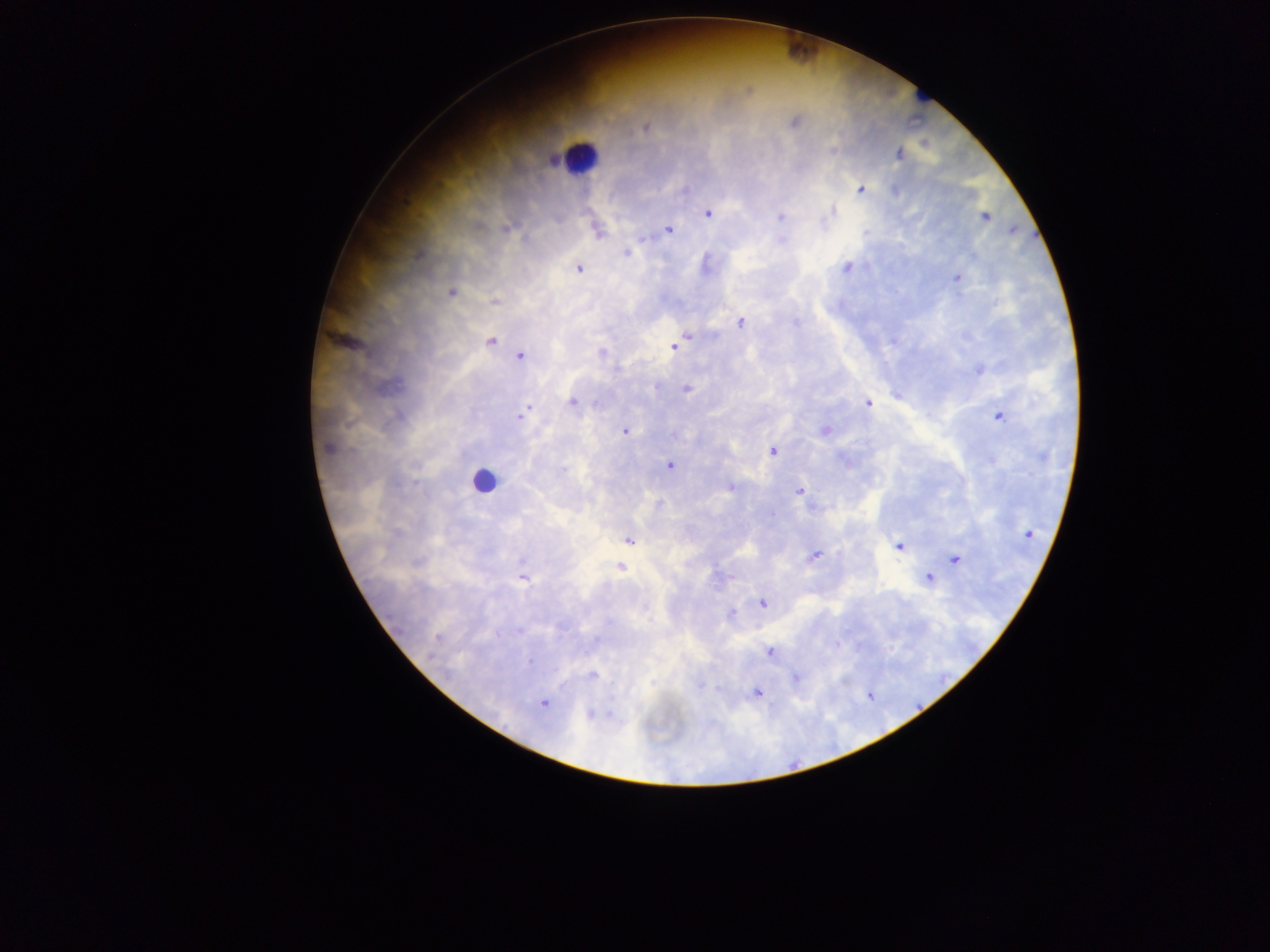
Approximate centers as x y in pixels.
Summary:
  - Leukocyte locations: 580 157; 483 481
  - Malaria parasite locations: 794 122; 646 128; 832 150; 899 154; 685 189; 862 190; 832 212; 708 213; 781 217; 985 217; 506 229; 1012 229; 668 230; 598 231; 625 253; 846 268; 578 269; 957 279; 451 293; 495 302; 741 322; 796 323; 687 336; 490 341; 674 346; 601 352; 520 356; 979 371; 686 389; 572 402; 868 403; 526 409; 521 415; 998 417; 624 431; 825 431; 673 435; 328 448; 773 451; 669 466; 563 470; 730 487; 799 491; 660 504; 771 514; 1027 535; 629 541; 899 546; 814 556; 956 560; 620 567; 522 578; 928 578; 762 603; 731 614; 519 632; 438 638; 769 652; 530 661; 592 675; 795 678; 702 686; 718 688; 756 693; 542 703; 591 713
  - Country: Ghana
  - Field of view: single
  - Capture: mobile-phone photograph through a microscope
  - Preparation: thick blood smear
  - Image size: 1270×952 pixels